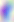

modality: micrograph
magnification: 400x
identification: Toxoplasma gondii